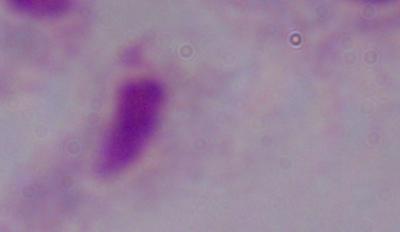
identification = trichomonad
magnification = 1000x
modality = photomicrograph